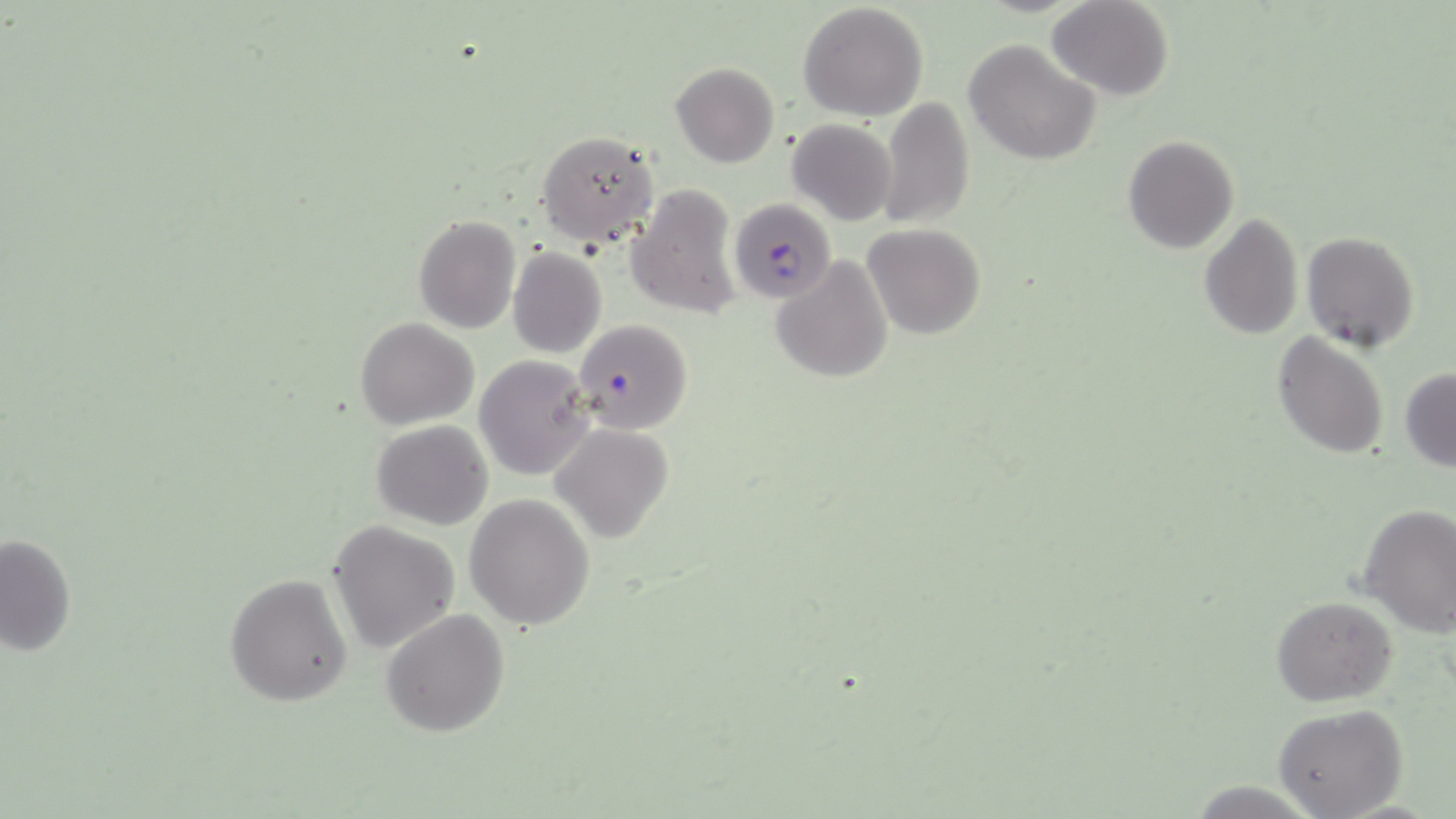
Summary:
  - Coordinate format: approximate bounding boxes as (x1, y1, x2, y2) in pixels
  - Plasmodium falciparum-infected red blood cell locations: (728, 198, 834, 307)
  - Uninfected red blood cell locations: (1049, 0, 1171, 101), (798, 2, 929, 119), (964, 38, 1100, 167), (669, 62, 779, 168), (877, 99, 975, 230), (787, 119, 897, 227), (535, 130, 661, 249), (1121, 135, 1238, 254), (628, 183, 742, 320), (1198, 212, 1304, 340), (413, 214, 522, 334), (862, 224, 985, 339), (1302, 231, 1419, 353), (508, 248, 607, 360), (771, 255, 893, 382), (356, 317, 479, 429), (572, 318, 694, 433), (1271, 333, 1390, 458), (474, 355, 595, 479), (1400, 368, 1456, 471), (371, 420, 493, 530), (551, 424, 673, 544), (466, 494, 595, 629), (1358, 504, 1455, 634), (329, 521, 460, 654), (0, 531, 77, 657), (224, 571, 353, 707), (1271, 595, 1397, 705), (380, 608, 511, 737), (1274, 704, 1407, 818)
  - Slide-level diagnosis: Plasmodium falciparum
  - Modality: optical microscopy
  - Stain: May-Grünwald-Giemsa
  - Field of view: one of a larger specimen
  - Image size: 1456×819 pixels
  - Preparation: thin blood smear
  - Magnification: 1000x